Locate every malaria parasite.
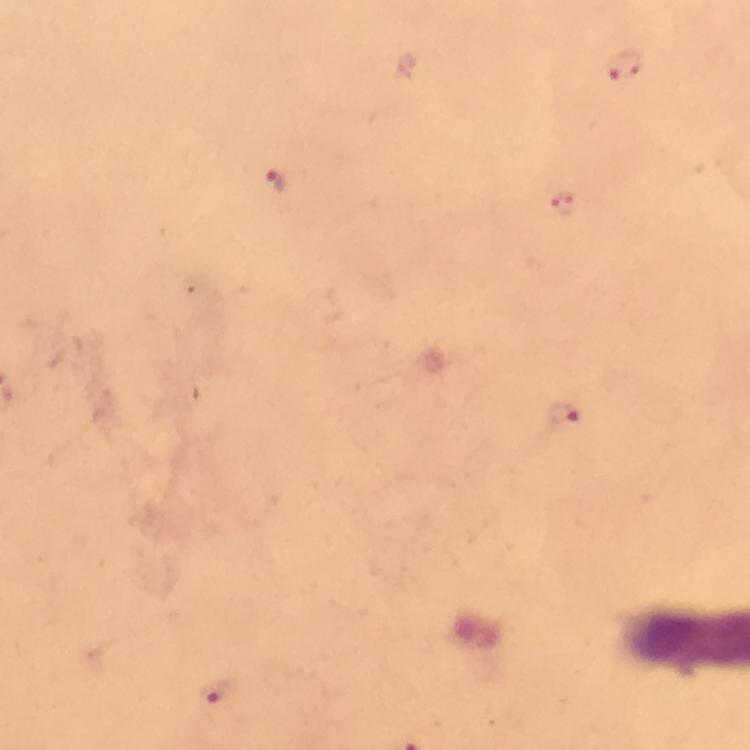
Approximate centers as (x, y) in pixels.
Malaria parasites: (623, 66), (276, 181), (561, 204), (564, 416), (214, 694).

From a malaria diagnostic workup. 100x magnification. Thick smear. Immersion oil was used. Giemsa-stained preparation. Photographed through the microscope with a smartphone camera. Image is 750×750 pixels. Cropped region of a single field of view.